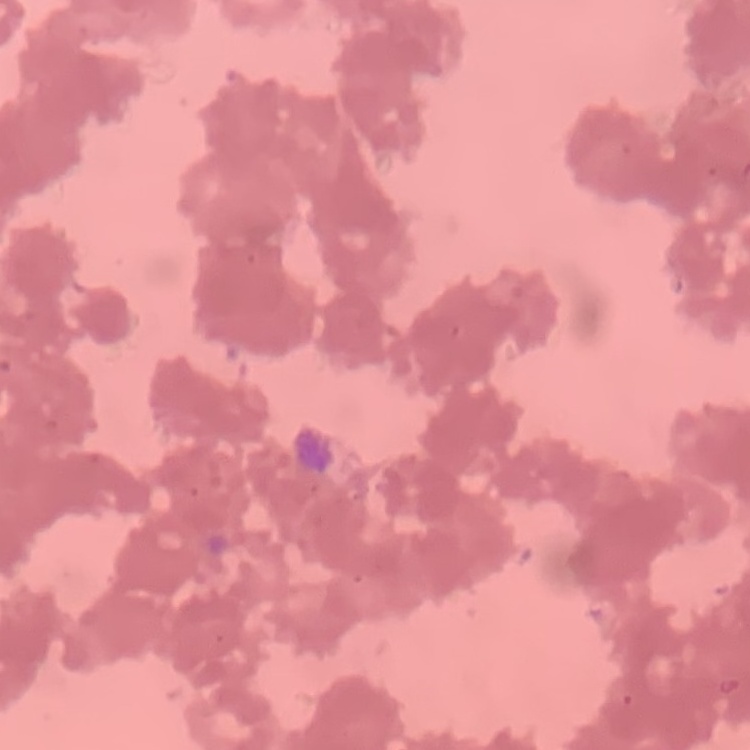 The erythrocytes exhibit rouleaux formation. Square crop of a larger photomicrograph. Stained with either Field's or Giemsa. Thin blood film.